State the blood parasite species.
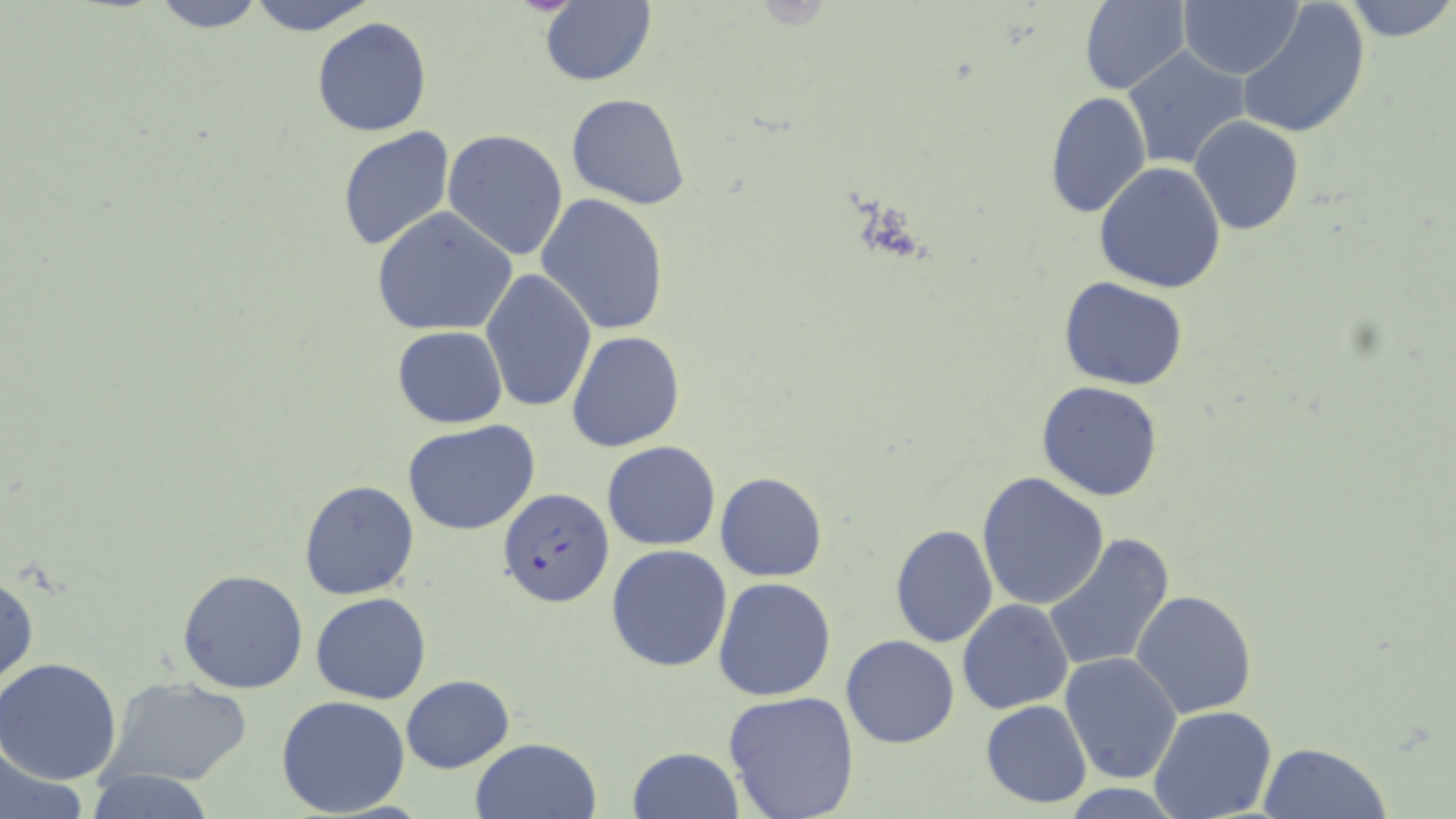

Plasmodium falciparum.

Approximate bounding boxes as [x1, y1, x2, y2] in pixels. Plasmodium falciparum-infected red blood cell locations: [498, 487, 613, 607]. Uninfected red blood cell locations: [146, 0, 274, 32], [241, 0, 381, 35], [1079, 0, 1189, 95], [1341, 0, 1455, 42], [1177, 1, 1303, 79], [537, 2, 657, 86], [1235, 2, 1372, 140], [311, 17, 433, 137], [1122, 45, 1254, 171], [1045, 90, 1152, 220], [566, 92, 692, 209], [1189, 116, 1305, 236], [336, 126, 455, 253], [441, 130, 569, 261], [1093, 161, 1226, 293], [536, 192, 671, 336], [371, 206, 518, 337], [480, 269, 597, 415], [1058, 276, 1188, 390], [393, 326, 507, 428], [566, 330, 686, 453], [1036, 380, 1164, 502], [402, 421, 541, 535], [603, 442, 721, 550], [714, 471, 828, 582], [977, 473, 1109, 611], [297, 480, 421, 600], [888, 523, 997, 648], [1042, 532, 1176, 675], [606, 545, 732, 671], [176, 569, 309, 695], [0, 571, 39, 693], [712, 576, 837, 702], [1131, 590, 1257, 718], [312, 593, 432, 704], [957, 598, 1073, 714], [841, 634, 960, 749], [1060, 652, 1183, 783], [0, 658, 124, 785], [103, 676, 254, 787], [401, 676, 516, 774], [722, 690, 860, 819], [276, 694, 411, 817], [981, 700, 1093, 810], [1148, 707, 1276, 819], [469, 737, 601, 819], [0, 739, 88, 819], [628, 743, 743, 817], [1258, 743, 1390, 819], [84, 770, 218, 819]. May-Grünwald-Giemsa-stained preparation. Captured at 1000x magnification. Thin blood smear. Single field of view. Light microscopy. Image is 1456×819 pixels.